Assess this cell for malaria.
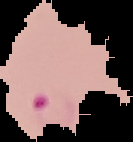
It is parasitized.

{
  "image_type": "segmented cell region with the area outside set to black",
  "image_size": "133×142 pixels",
  "preparation": "thin blood film"
}